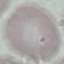

Summary:
  - Malaria status: uninfected
  - Preparation: thin smear
  - Capture: smartphone through the microscope eyepiece
  - Image type: cell patch, automatically extracted from a larger field of view and resized to 64 × 64 pixels
  - Stain: Giemsa